Classify this cell by malaria status.
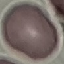

It is uninfected.

Summary:
  - Stain: Giemsa
  - Preparation: thin smear
  - Capture: smartphone through the microscope eyepiece
  - Image type: automatically extracted cell patch, resized to 64 × 64 pixels